Classify this cell by malaria status.
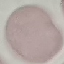
It is uninfected.

{
  "stain": "Giemsa",
  "preparation": "thin blood film",
  "image_type": "cell patch, automatically extracted from a larger field of view and resized to 64 × 64 pixels",
  "capture": "smartphone camera at the microscope eyepiece"
}